Identify the parasite.
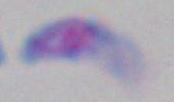
Toxoplasma gondii.

{
  "modality": "photomicrograph",
  "magnification": "1000x"
}